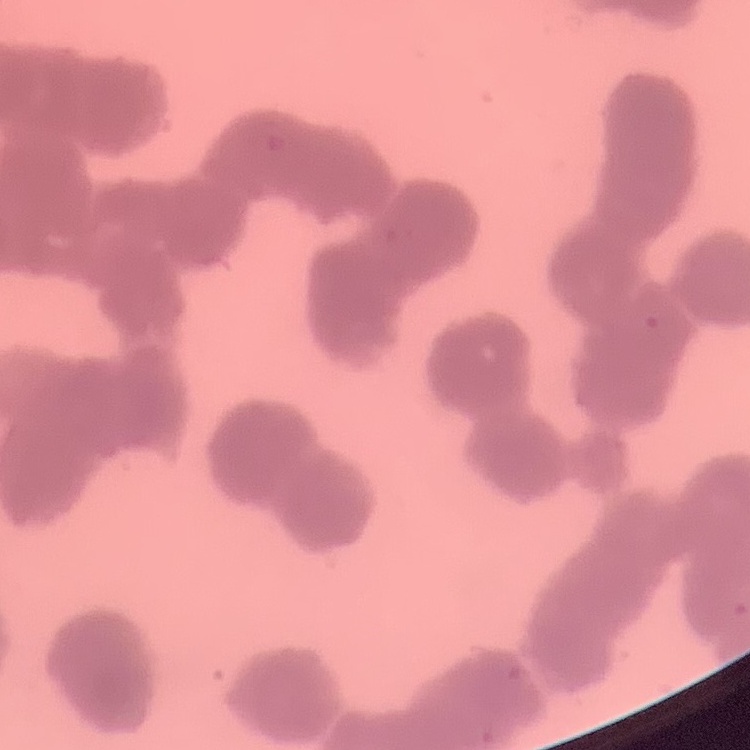
Summary:
  - Red blood cell morphology: rouleaux formation
  - Preparation: thin peripheral smear
  - Image type: one tile cut from a larger photomicrograph
  - Stain: Field's or Giemsa